Classify this cell by malaria status.
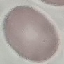
It is uninfected.

Automatically extracted cell patch, resized to 64 × 64 pixels. Thin blood film. Giemsa-stained preparation. Photographed with a smartphone camera at the microscope eyepiece.